Describe the morphology of the red blood cells.
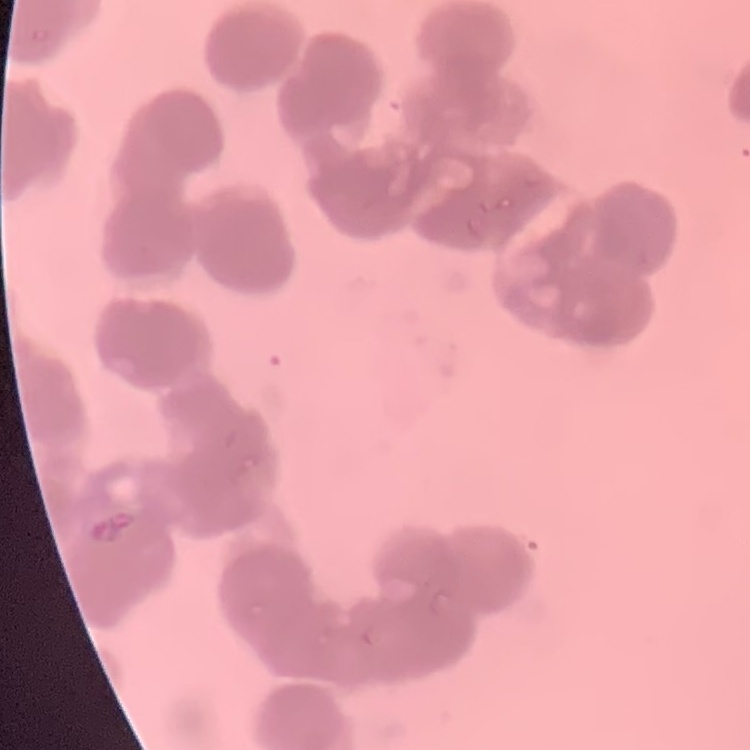
They show rouleaux formation.

One tile cut from a larger photomicrograph. Thin blood smear. Stained with either Field's or Giemsa.